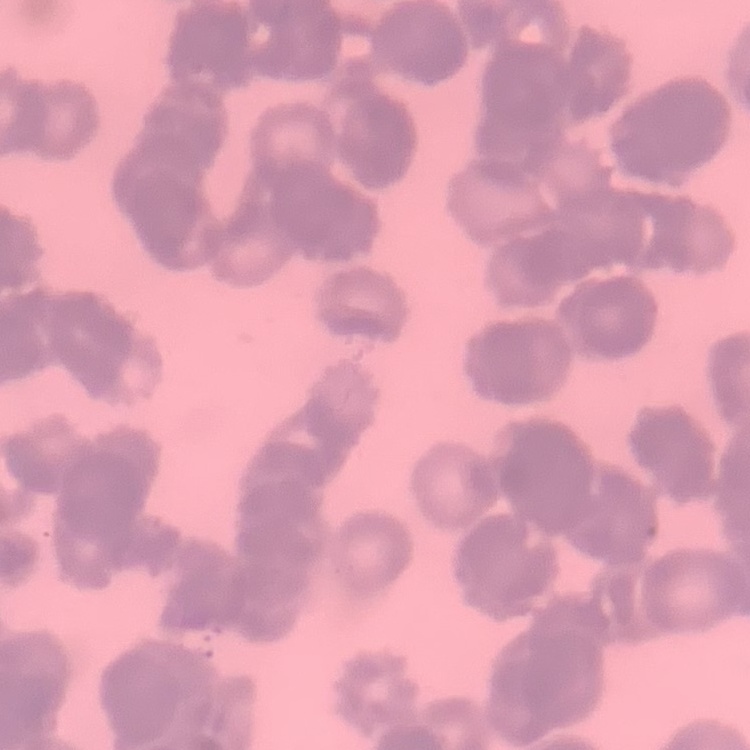

The red blood cells exhibit rouleaux formation. Square crop of a larger photomicrograph. Stained with either Field's or Giemsa. Thin blood film.